Classify this cell by malaria status.
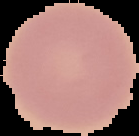

Uninfected.

From a thin blood smear. The area outside the segmented cell region is set to black. Image is 139×136 pixels.